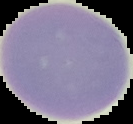 Image is 133×124 pixels. Segmented cell region on a black background. Malaria status: uninfected. From a thin blood smear.